State which parasite is depicted.
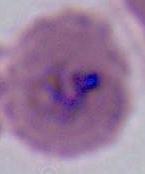
Plasmodium.

magnification: 400x or 1000x
modality: micrograph